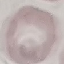
Malaria status: uninfected. Giemsa stain. Cell patch, automatically extracted from a larger field of view and resized to 64 × 64 pixels. Thin blood film. Photographed with a smartphone camera at the microscope eyepiece.